Name the cell type shown.
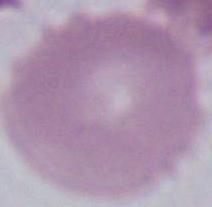

An erythrocyte.

Summary:
  - Magnification: 1000x
  - Modality: micrograph